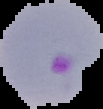

Summary:
  - Image size: 103×109 pixels
  - Malaria status: parasitized
  - Preparation: thin blood smear
  - Image type: segmented cell region with the area outside set to black